Outline each uninfected red blood cell.
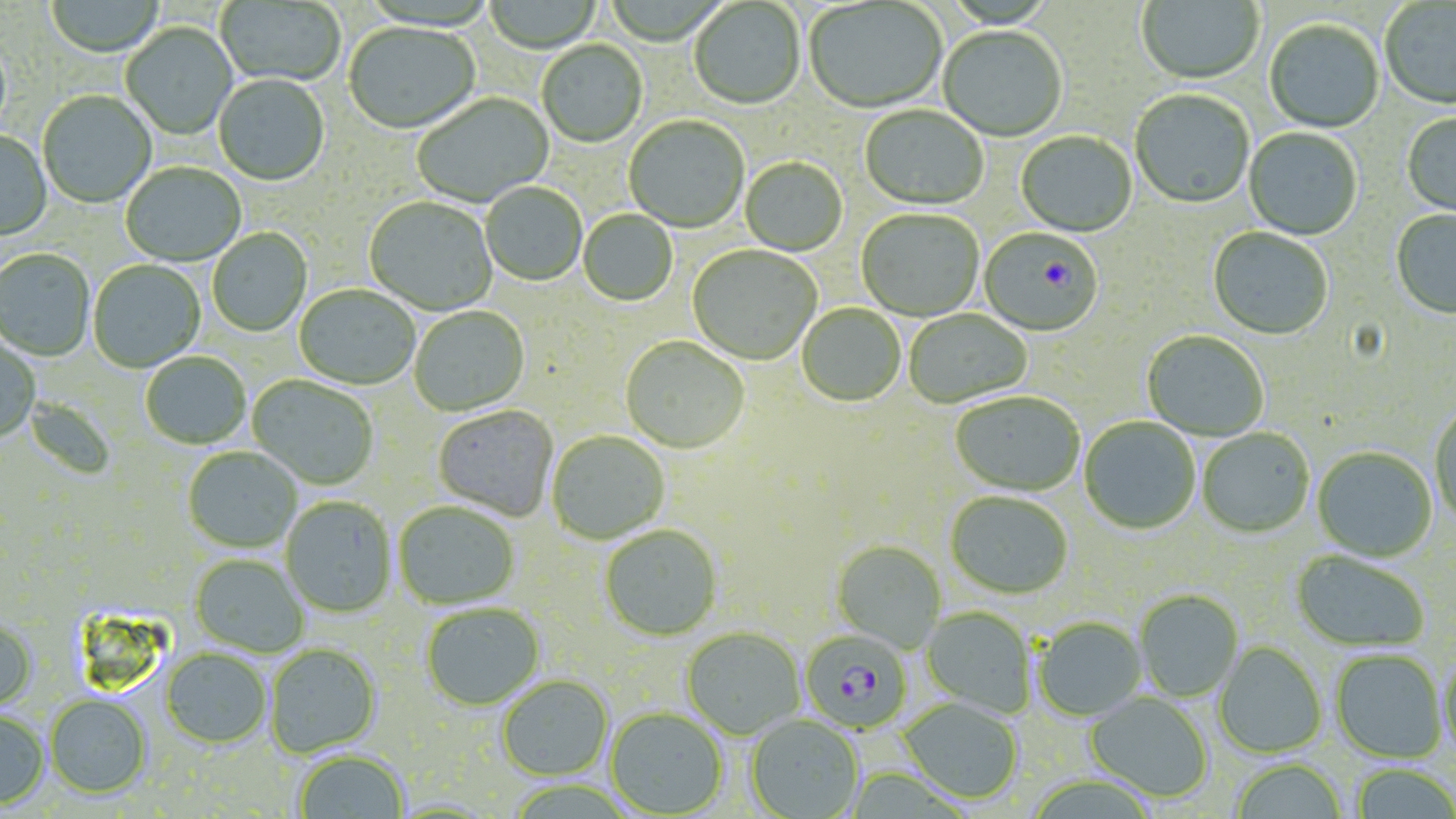

Approximate bounding boxes as (x1,y1)-(x2,y2) corner pairs in pixels.
Uninfected red blood cells: (483,0)-(603,54), (1136,0)-(1264,87), (45,1)-(165,59), (217,1)-(346,88), (689,1)-(805,111), (804,1)-(947,116), (1380,1)-(1456,112), (1264,21)-(1385,134), (121,22)-(237,141), (344,23)-(480,136), (938,28)-(1067,143), (537,41)-(648,148), (214,75)-(330,188), (38,91)-(157,209), (1130,91)-(1255,211), (413,93)-(555,208), (859,107)-(988,212), (1401,113)-(1456,220), (624,117)-(749,234), (1243,128)-(1362,241), (0,131)-(52,242), (1016,132)-(1137,238), (740,158)-(848,257), (120,164)-(246,267), (481,183)-(587,287), (364,198)-(498,316), (1391,209)-(1456,319), (578,210)-(678,307), (856,210)-(984,322), (208,228)-(312,337), (1208,228)-(1333,341), (687,245)-(822,366), (0,249)-(95,362), (88,260)-(206,373), (294,286)-(420,390), (797,305)-(905,408), (409,307)-(530,417), (903,309)-(1032,410), (1142,332)-(1269,442), (0,337)-(41,444), (620,338)-(749,455), (141,353)-(251,450), (247,375)-(378,490), (950,393)-(1084,498), (23,396)-(117,481), (433,406)-(558,521), (1429,406)-(1456,528), (1079,418)-(1201,535), (1197,429)-(1314,539), (547,431)-(670,544), (183,447)-(302,554), (1312,448)-(1437,563), (945,494)-(1073,600), (281,497)-(397,618), (393,502)-(519,610), (600,526)-(721,642), (832,541)-(945,653), (1290,551)-(1430,654), (190,554)-(308,657), (1134,591)-(1244,703), (421,603)-(545,710), (922,607)-(1037,718), (0,617)-(37,711), (1033,618)-(1147,722), (681,629)-(805,740), (1214,643)-(1326,758), (266,644)-(381,758), (161,649)-(270,748), (1330,651)-(1447,765), (1438,653)-(1456,765), (497,675)-(613,781), (1085,693)-(1212,804), (44,694)-(152,798), (898,698)-(1022,805), (606,709)-(727,817), (0,710)-(48,808), (746,716)-(864,819), (294,751)-(409,818), (1231,760)-(1347,819), (1351,765)-(1456,819).

Plasmodium falciparum-infected red blood cell locations: (979,231)-(1102,338), (800,632)-(912,733). Slide-level diagnosis: Plasmodium falciparum. Captured at 1000x magnification. Optical microscopy. May-Grünwald-Giemsa stain. Image is 1456×819 pixels. Thin blood film. One field of a larger specimen.